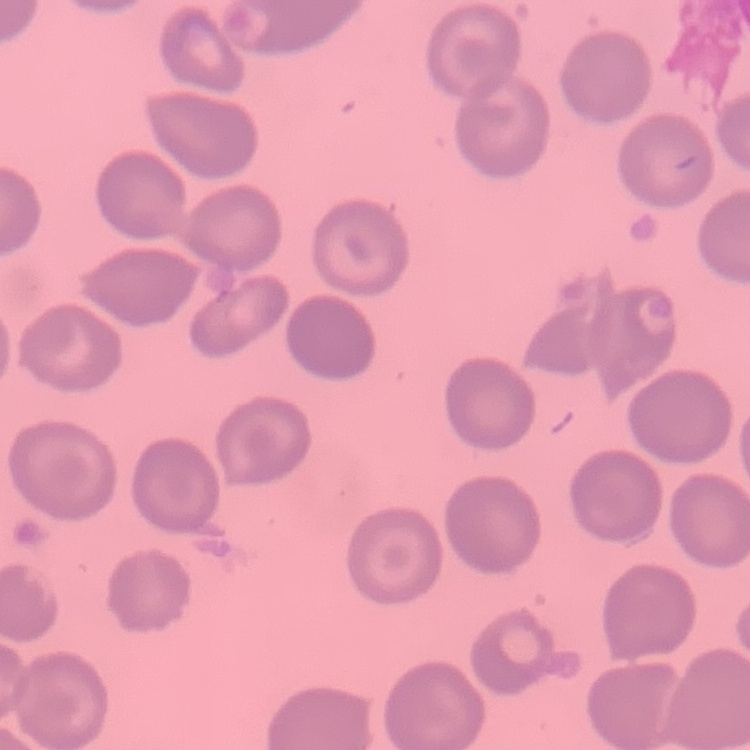
The erythrocytes exhibit no rouleaux formation. One tile cut from a larger photomicrograph. Stained with either Field's or Giemsa. Thin blood film.